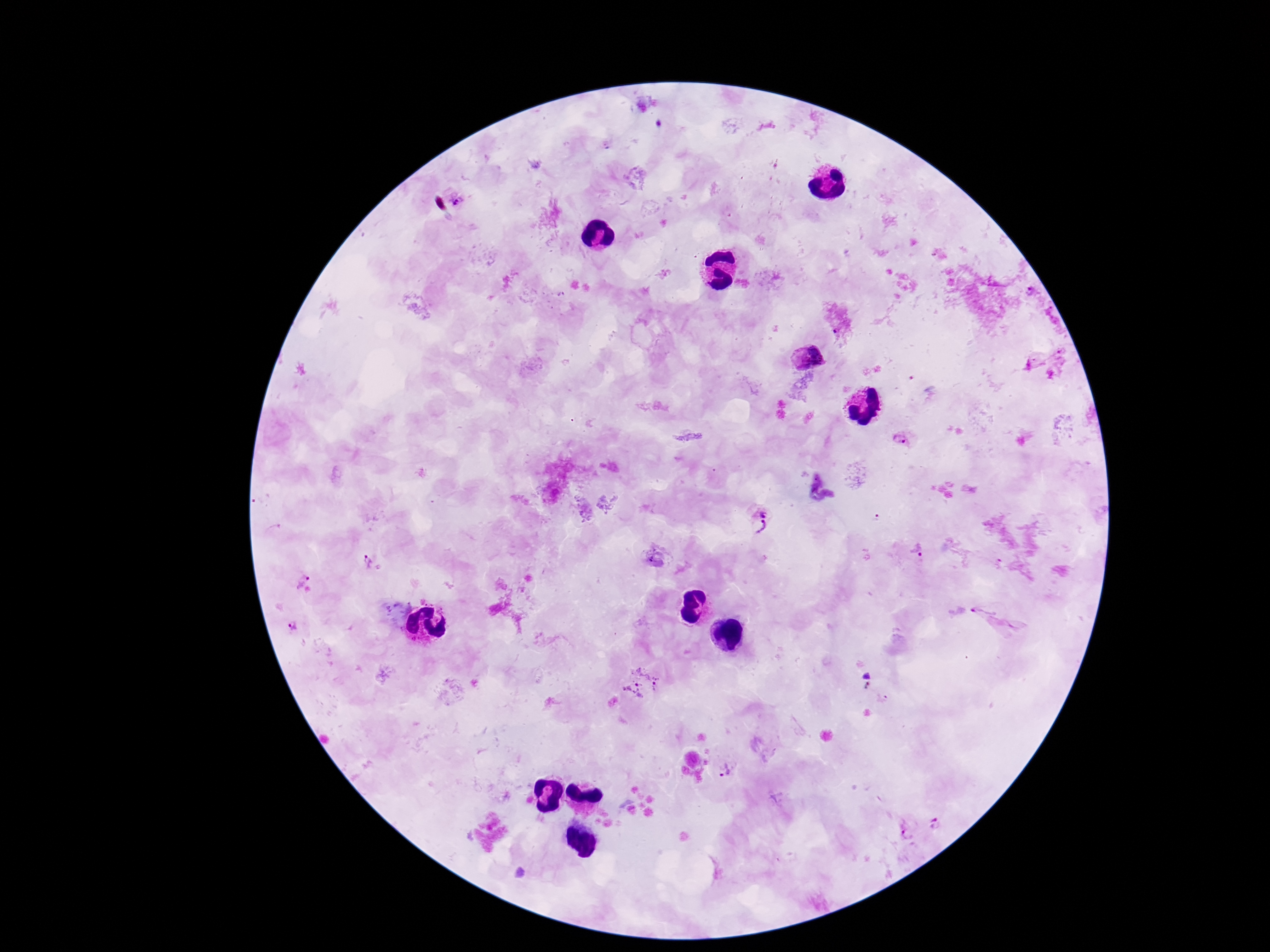

Approximate centers as [x, y] in pixels. Plasmodium parasite locations: [459, 201], [1032, 292], [808, 357], [900, 439], [762, 508], [762, 528], [918, 551], [371, 563], [300, 575], [988, 606], [291, 627], [643, 680], [726, 769], [936, 821], [908, 830]. One field from this slide. 100x magnification. Patient malaria status: positive. Giemsa stain. Thick peripheral-blood smear. Image is 1270×952 pixels. Photographed through the microscope eyepiece with a smartphone camera.